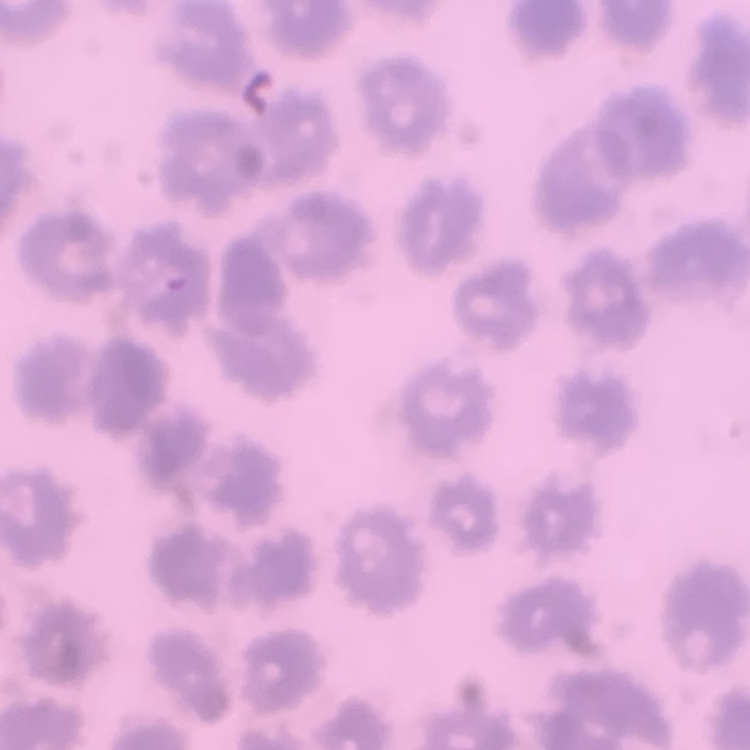
erythrocyte_morphology: no rouleaux formation
stain: Field's or Giemsa
preparation: thin peripheral smear
image_type: one tile cut from a larger photomicrograph